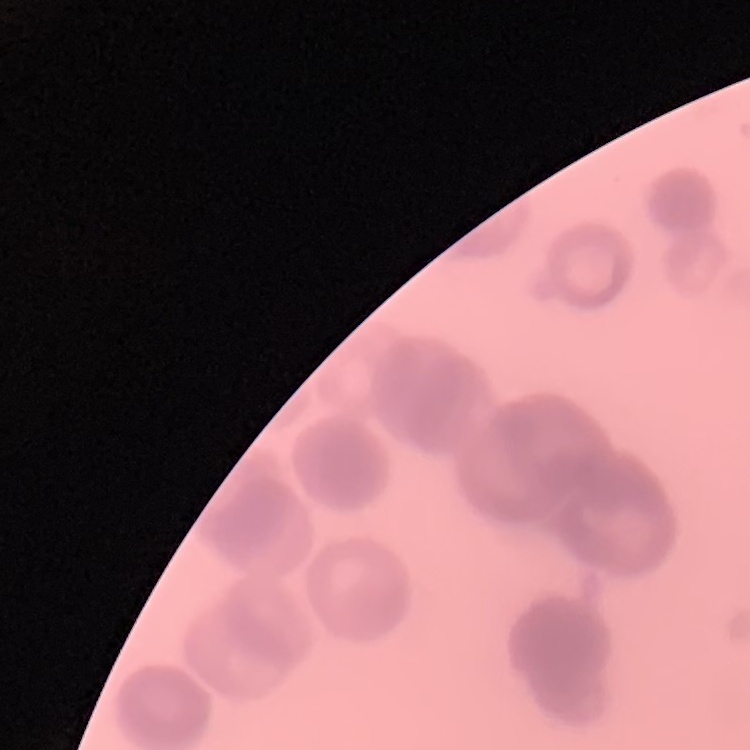 The erythrocytes exhibit rouleaux formation. Thin blood smear. Square crop of a larger photomicrograph. Stained with either Field's or Giemsa.